Name the parasite shown.
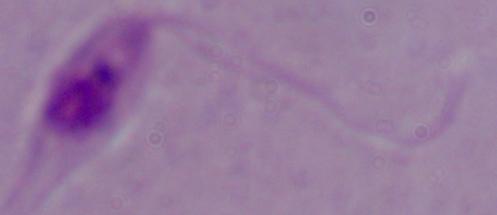

Leishmania.

Summary:
  - Modality: micrograph
  - Magnification: 1000x